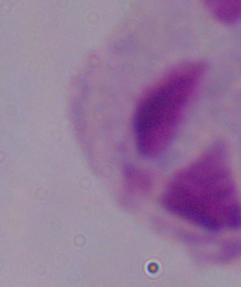
identification = trichomonad
magnification = 1000x
modality = photomicrograph